Assess this cell for malaria.
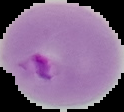
Parasitized.

From a thin blood smear. Cell region segmented out of the field of view; the surrounding area is masked to black. Image is 124×112 pixels.